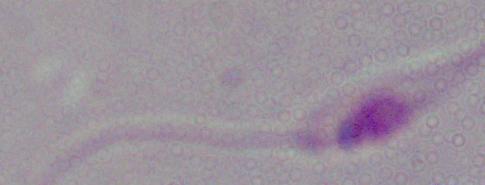

Summary:
  - Identification: Leishmania
  - Magnification: 1000x
  - Modality: micrograph